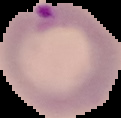

{
  "malaria_status": "parasitized",
  "image_size": "121×118 pixels",
  "image_type": "segmented cell region on a black background",
  "preparation": "thin blood film"
}